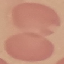

Result: negative for malaria parasites. Cell patch, automatically extracted from a larger field of view and resized to 64 × 64 pixels. Thin blood film. Photographed with a smartphone camera at the microscope eyepiece. Giemsa-stained preparation.